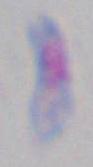
Photomicrograph. Captured at 1000x magnification. Toxoplasma gondii is shown.